Classify this cell by malaria status.
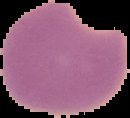
Parasitized.

From a thin blood smear. Cell region segmented out of the field of view; the surrounding area is masked to black. Image is 130×118 pixels.